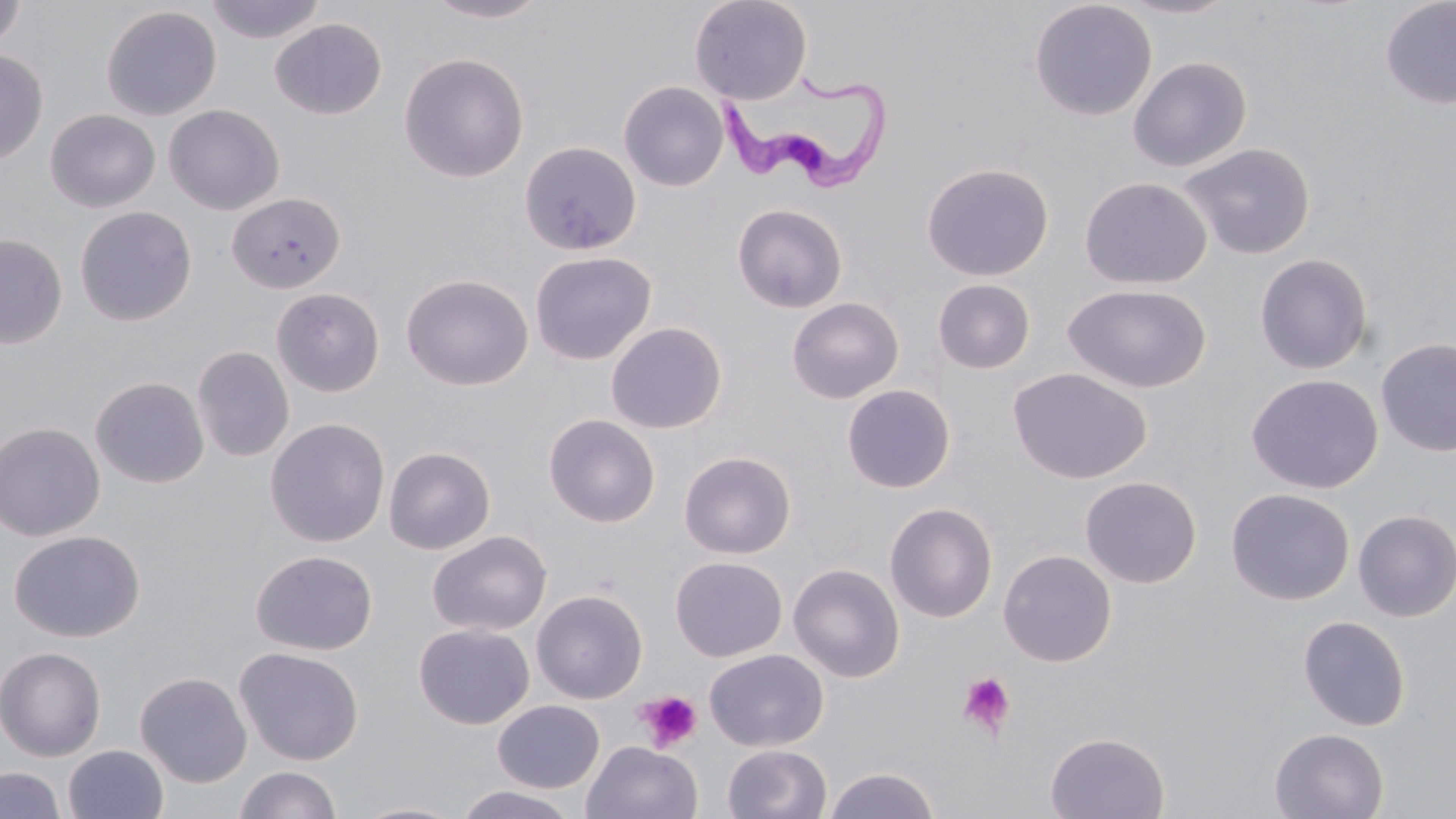

Approximate bounding boxes as (x1, y1, x2, y2) in pixels. Trypanosoma brucei locations: (727, 78, 892, 191). Platelet locations: (957, 670, 1016, 738), (635, 690, 703, 752). Uninfected red blood cell locations: (0, 0, 27, 54), (203, 0, 328, 44), (424, 0, 552, 23), (688, 0, 812, 105), (1029, 0, 1158, 121), (1115, 0, 1241, 19), (1379, 0, 1456, 110), (100, 5, 222, 120), (269, 18, 387, 119), (0, 49, 48, 165), (399, 53, 529, 183), (1128, 56, 1252, 172), (618, 81, 729, 192), (163, 104, 285, 216), (45, 109, 160, 213), (518, 141, 642, 256), (1178, 142, 1317, 260), (921, 162, 1054, 281), (1079, 177, 1212, 289), (226, 192, 345, 293), (732, 203, 847, 313), (74, 206, 197, 326), (0, 233, 67, 349), (529, 250, 657, 366), (1254, 253, 1374, 375), (401, 274, 534, 390), (933, 279, 1036, 374), (1063, 284, 1212, 394), (271, 288, 384, 398), (786, 297, 904, 404), (605, 322, 727, 434), (1376, 338, 1456, 457), (191, 346, 294, 463), (1008, 367, 1152, 484), (1246, 373, 1383, 494), (90, 376, 209, 489), (842, 384, 955, 493), (543, 414, 660, 528), (264, 417, 390, 548), (0, 422, 105, 542), (383, 446, 496, 555), (679, 450, 796, 559), (1079, 476, 1202, 589), (1225, 488, 1355, 606), (884, 502, 998, 623), (1352, 509, 1456, 622), (8, 529, 145, 642), (427, 530, 552, 637), (997, 549, 1117, 667), (250, 550, 378, 656), (670, 556, 787, 662), (788, 562, 905, 682), (531, 589, 648, 704), (1297, 615, 1411, 731), (413, 623, 534, 729), (0, 646, 106, 761), (234, 647, 364, 765), (704, 648, 828, 752), (135, 671, 252, 787), (492, 700, 605, 793), (1269, 727, 1390, 819), (1044, 732, 1170, 818), (581, 740, 703, 819), (723, 744, 832, 819), (62, 745, 168, 819), (234, 765, 342, 819), (0, 766, 65, 819), (823, 767, 941, 819), (449, 786, 583, 819), (349, 801, 469, 819). Slide-level diagnosis: Trypanosoma brucei. Captured at 1000x magnification. Single field of view. Light microscopy. May-Grünwald-Giemsa stain. Thin blood smear. Image is 1456×819 pixels.